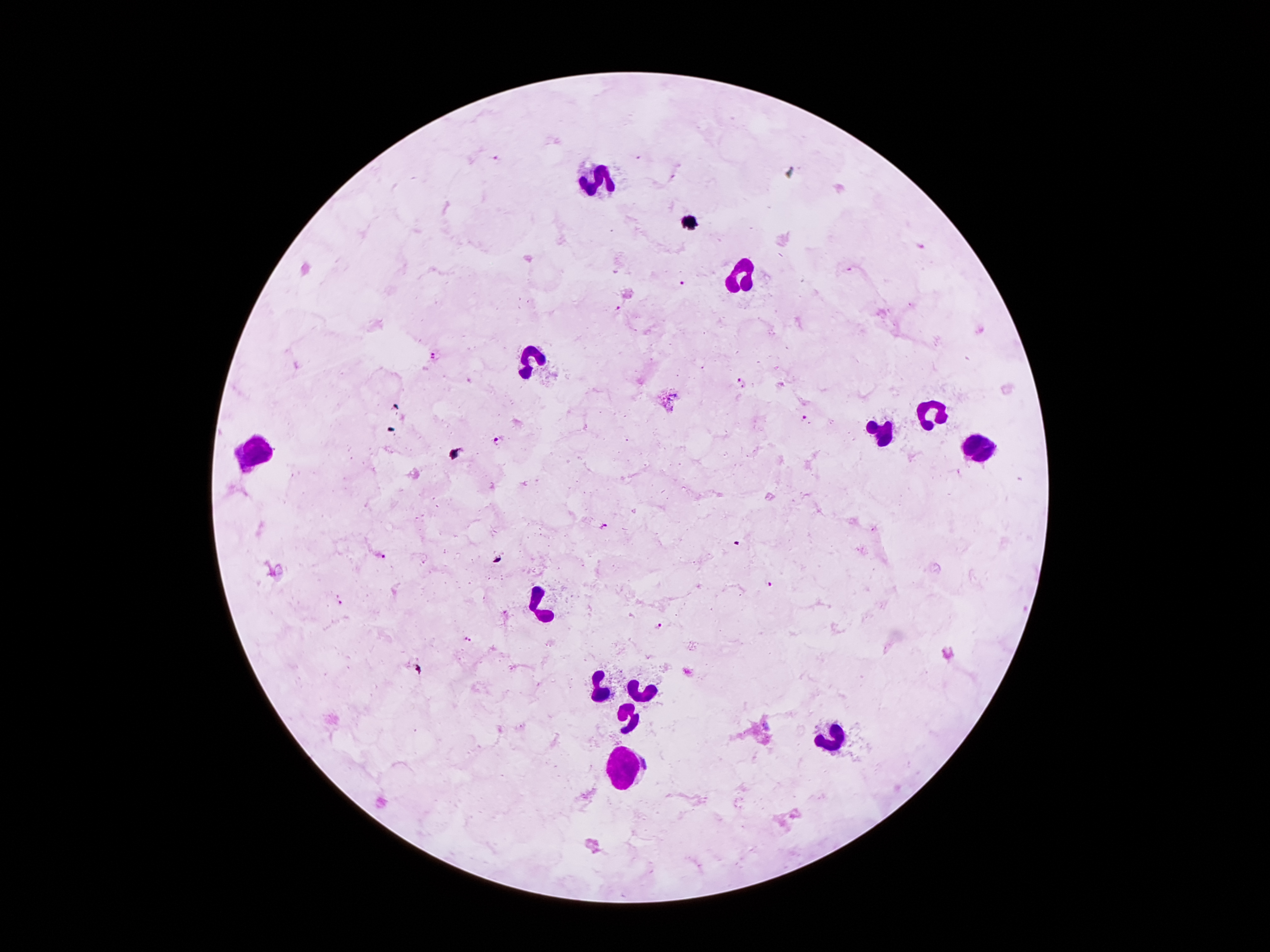

Approximate centers as [x, y] in pixels.
Summary:
  - Leukocyte locations: [596, 180], [744, 278], [535, 357], [930, 412], [883, 432], [260, 449], [976, 451], [537, 607], [596, 691], [644, 692], [626, 712], [835, 733], [624, 767]
  - Plasmodium parasite locations: [494, 156], [923, 247], [681, 283], [620, 308], [434, 355], [741, 383], [805, 418], [497, 439], [603, 527], [381, 555], [767, 584], [340, 603], [660, 628], [468, 638]
  - Field of view: one from this slide
  - Stain: Giemsa
  - Magnification: 100x
  - Patient malaria status: infected with Plasmodium falciparum
  - Image size: 1270×952 pixels
  - Preparation: thick peripheral-blood smear
  - Capture: smartphone camera through the microscope eyepiece